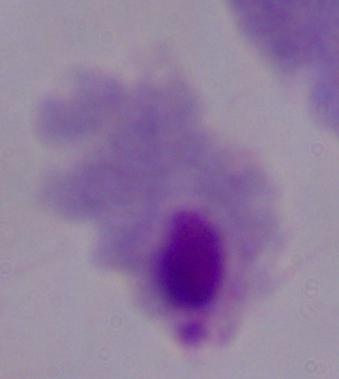

modality = photomicrograph
magnification = 1000x
identification = trichomonad